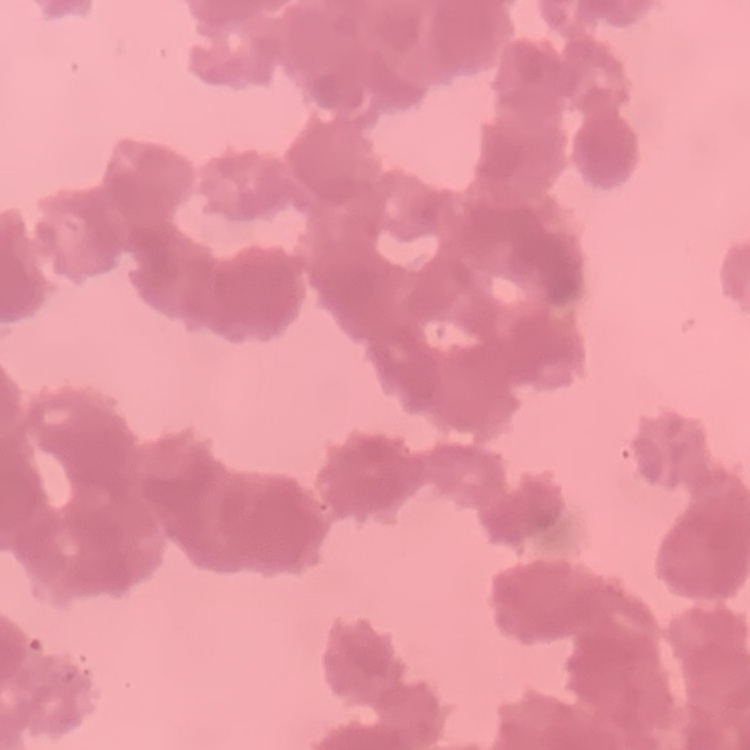

The red blood cells show rouleaux formation. One tile cut from a larger photomicrograph. Stained with either Field's or Giemsa. Thin peripheral smear.